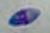

Summary:
  - Modality: photomicrograph
  - Magnification: 1000x
  - Identification: Toxoplasma gondii